Name the parasite shown.
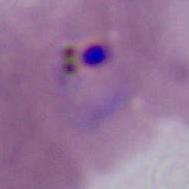

This is Plasmodium.

magnification = 400x or 1000x
modality = micrograph